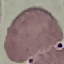

Malaria status: uninfected. Giemsa-stained preparation. Thin blood film. Automatically extracted cell patch, resized to 64 × 64 pixels. Photographed with a smartphone camera at the microscope eyepiece.